Describe the morphology of the red blood cells.
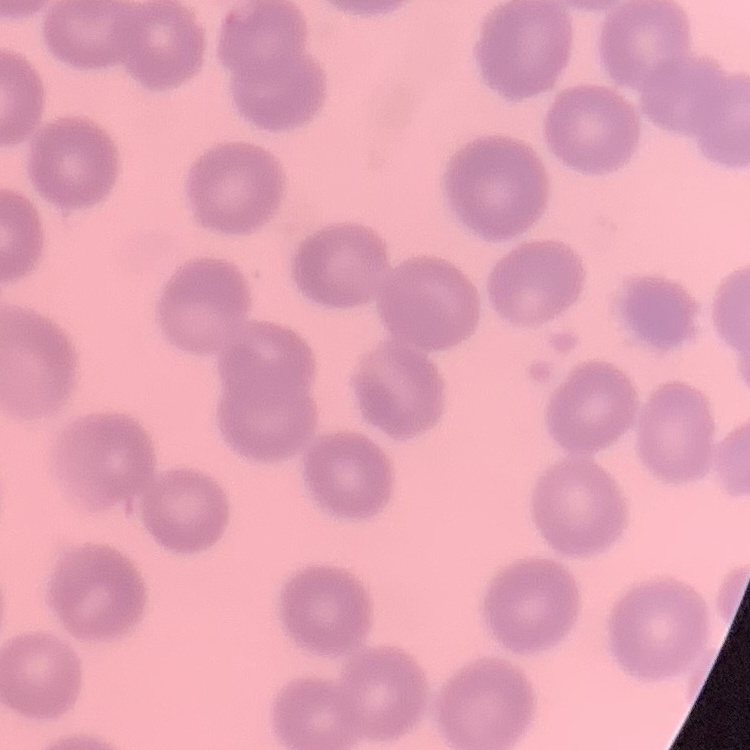
No rouleaux formation.

image type = one tile cut from a larger photomicrograph
preparation = thin peripheral smear
stain = Field's or Giemsa